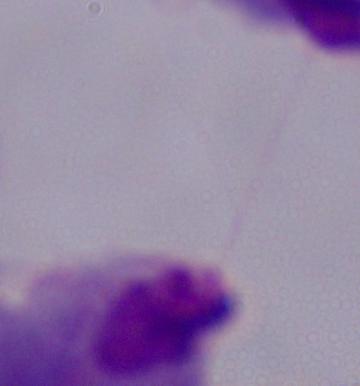
identification = trichomonad
modality = photomicrograph
magnification = 1000x